Give the position of every Plasmodium parasite visible.
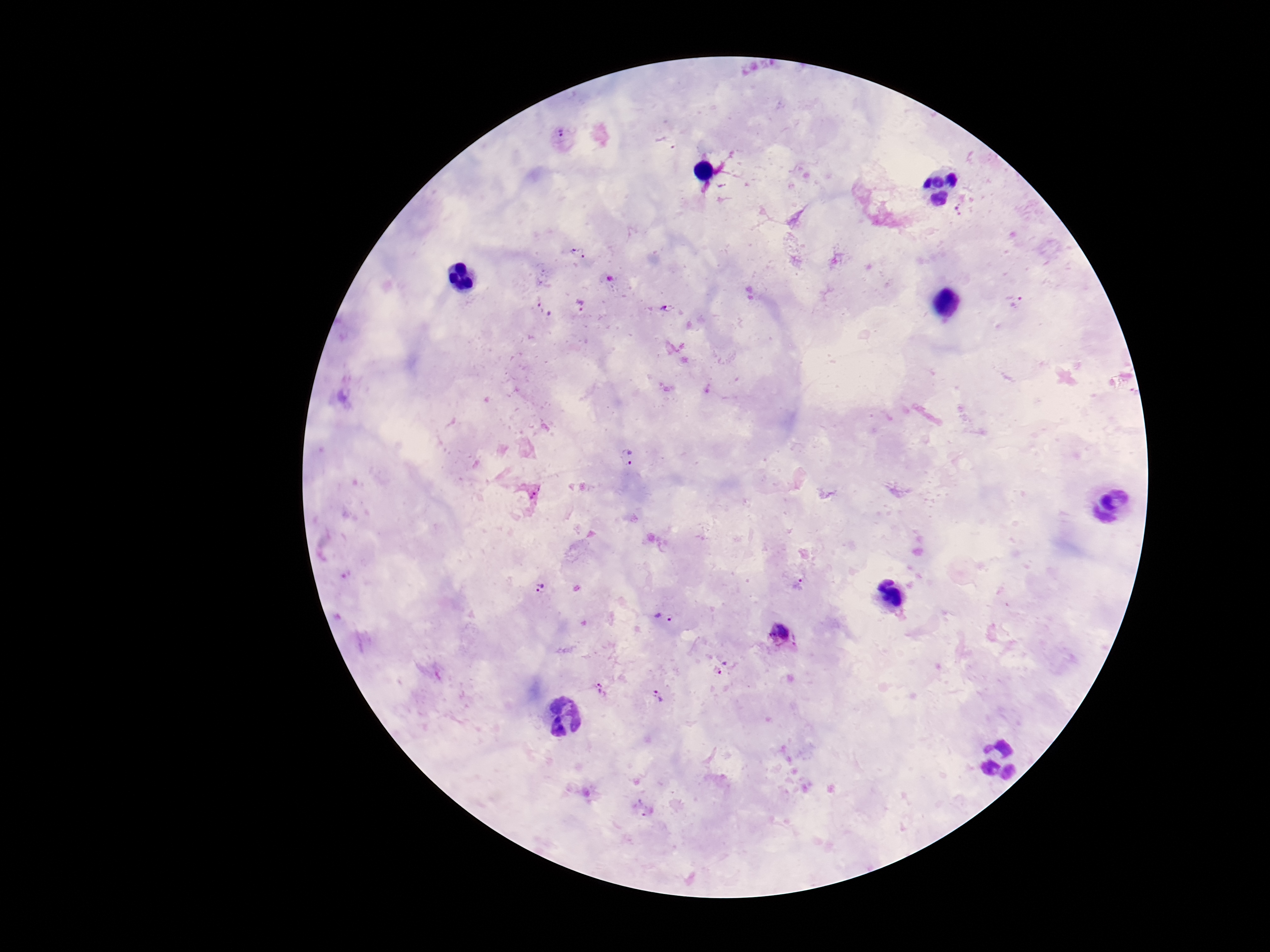
Approximate object centers, in pixels from the top-left corner.
Plasmodium parasites: (x=563, y=137), (x=667, y=142), (x=722, y=185), (x=959, y=209), (x=578, y=253), (x=610, y=278), (x=1016, y=302), (x=581, y=305), (x=669, y=308), (x=543, y=309), (x=629, y=455), (x=889, y=581), (x=799, y=585), (x=879, y=587), (x=539, y=590), (x=660, y=620), (x=782, y=637), (x=723, y=667), (x=601, y=690), (x=658, y=696), (x=643, y=808).

Patient malaria status: infected. 100x magnification. Thick peripheral-blood smear. Image is 1270×952 pixels. Giemsa stain. One field from this slide. Photographed through the microscope eyepiece with a smartphone camera.